State which parasite is depicted.
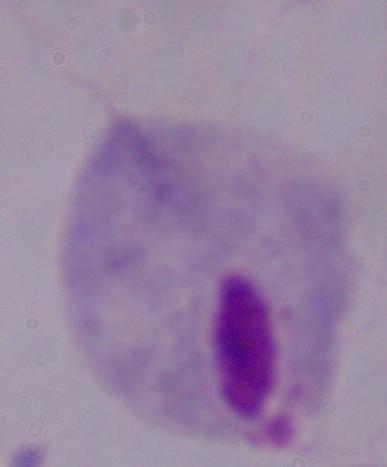

A trichomonad.

modality = photomicrograph
magnification = 1000x